Comment on the morphology of the erythrocytes.
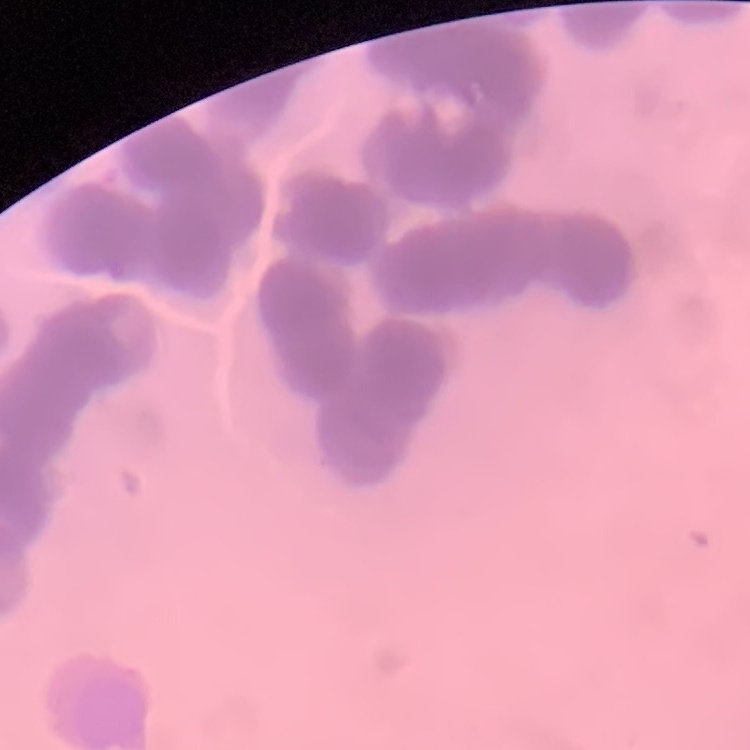

They show rouleaux formation.

Summary:
  - Preparation: thin blood smear
  - Image type: one tile cut from a larger photomicrograph
  - Stain: Field's or Giemsa